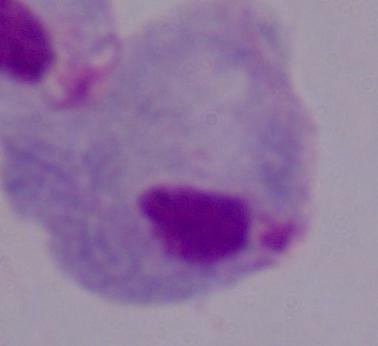

A trichomonad is shown. 1000x magnification. Micrograph.